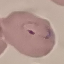
Summary:
  - Result: malaria parasites identified
  - Capture: smartphone through the microscope eyepiece
  - Stain: Giemsa
  - Preparation: thin blood film
  - Image type: automatically extracted cell patch, resized to 64 × 64 pixels